Comment on the morphology of the red blood cells.
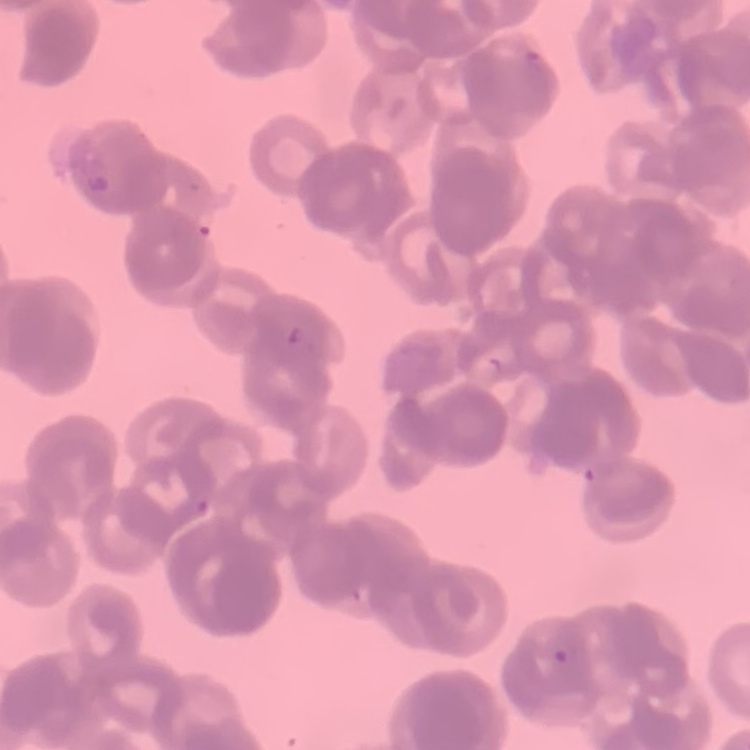
Rouleaux formation.

One tile cut from a larger photomicrograph. Thin peripheral smear. Stained with either Field's or Giemsa.